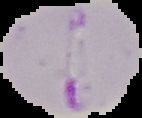
image type = segmented cell region with the area outside set to black
image size = 142×118 pixels
preparation = thin blood film
malaria status = parasitized